Identify the cell.
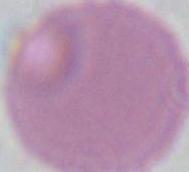

An erythrocyte.

Summary:
  - Magnification: 1000x
  - Modality: micrograph